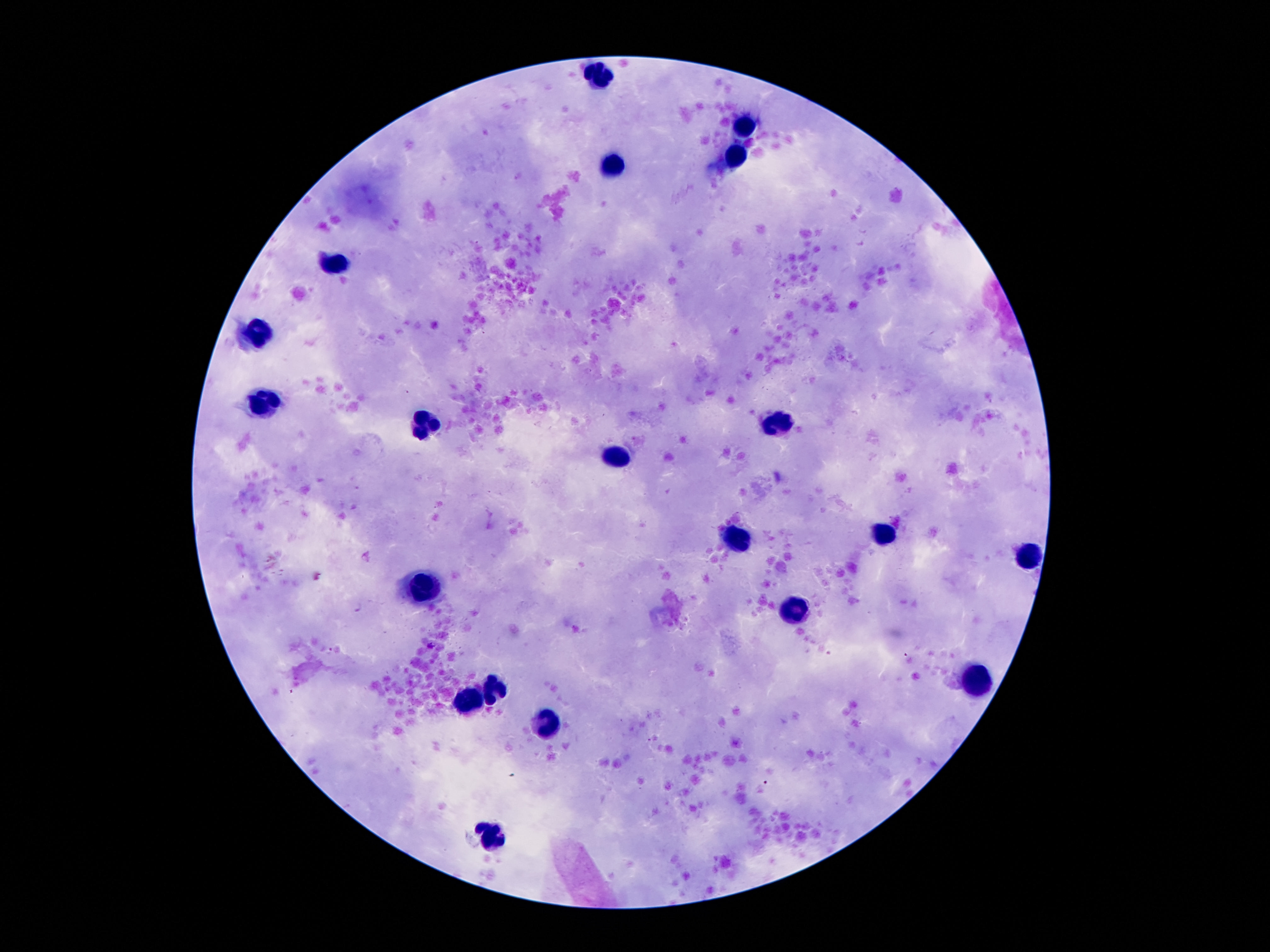

{
  "image_size": "1270×952 pixels",
  "patient_malaria_status": "uninfected",
  "field_of_view": "single",
  "leukocyte_locations": "approximate centers as {x, y} in pixels: {599, 77}, {743, 125}, {736, 156}, {611, 163}, {336, 263}, {259, 334}, {264, 410}, {429, 422}, {776, 427}, {617, 454}, {879, 533}, {738, 542}, {1028, 559}, {422, 588}, {797, 610}, {976, 679}, {493, 688}, {472, 699}, {545, 722}, {490, 836}",
  "preparation": "thick peripheral-blood smear",
  "magnification": "100x",
  "stain": "Giemsa",
  "capture": "smartphone camera through the microscope eyepiece"
}